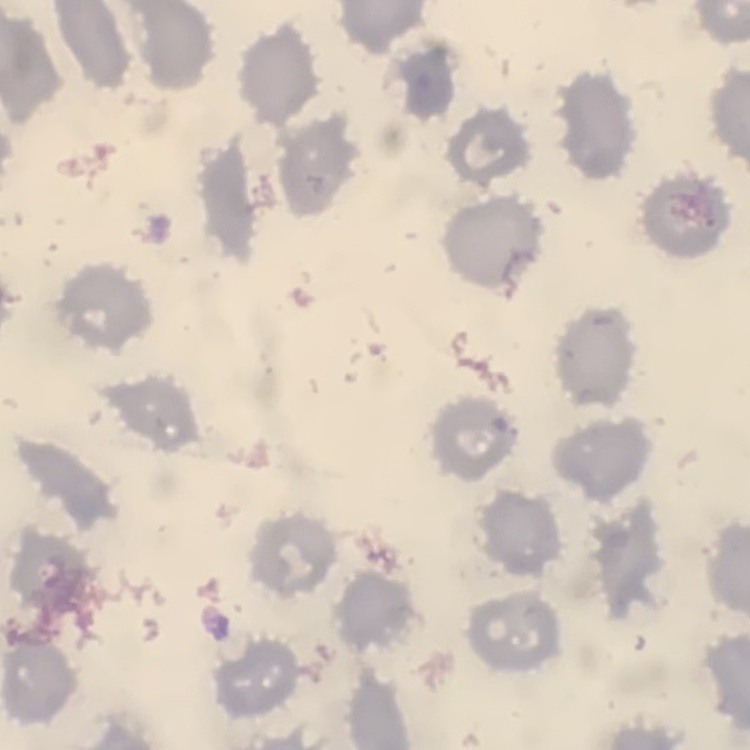

The red blood cells exhibit no rouleaux formation. Stained with either Field's or Giemsa. Thin blood smear. One tile cut from a larger photomicrograph.